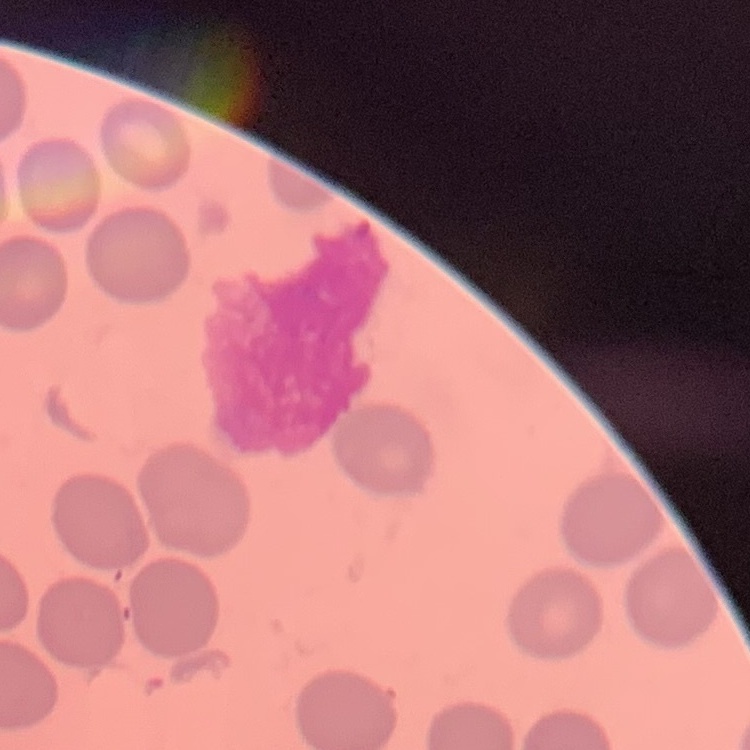

The red blood cells exhibit no rouleaux formation. Thin blood smear. Square crop of a larger photomicrograph. Field's or Giemsa stain.